State which parasite is depicted.
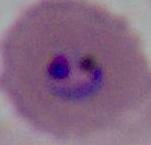

Plasmodium.

Summary:
  - Magnification: 400x or 1000x
  - Modality: photomicrograph